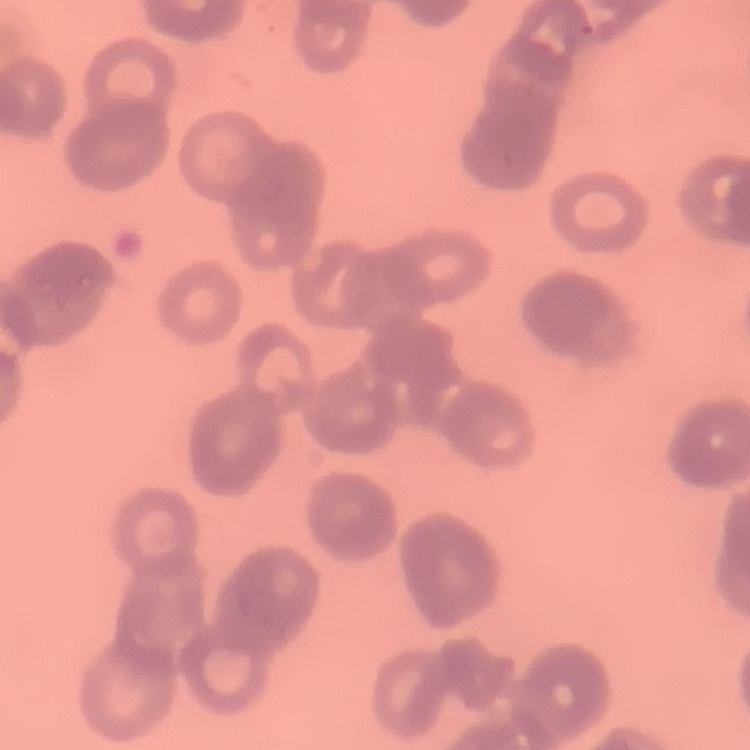
erythrocyte morphology = rouleaux formation
image type = one tile cut from a larger photomicrograph
preparation = thin blood film
stain = Field's or Giemsa